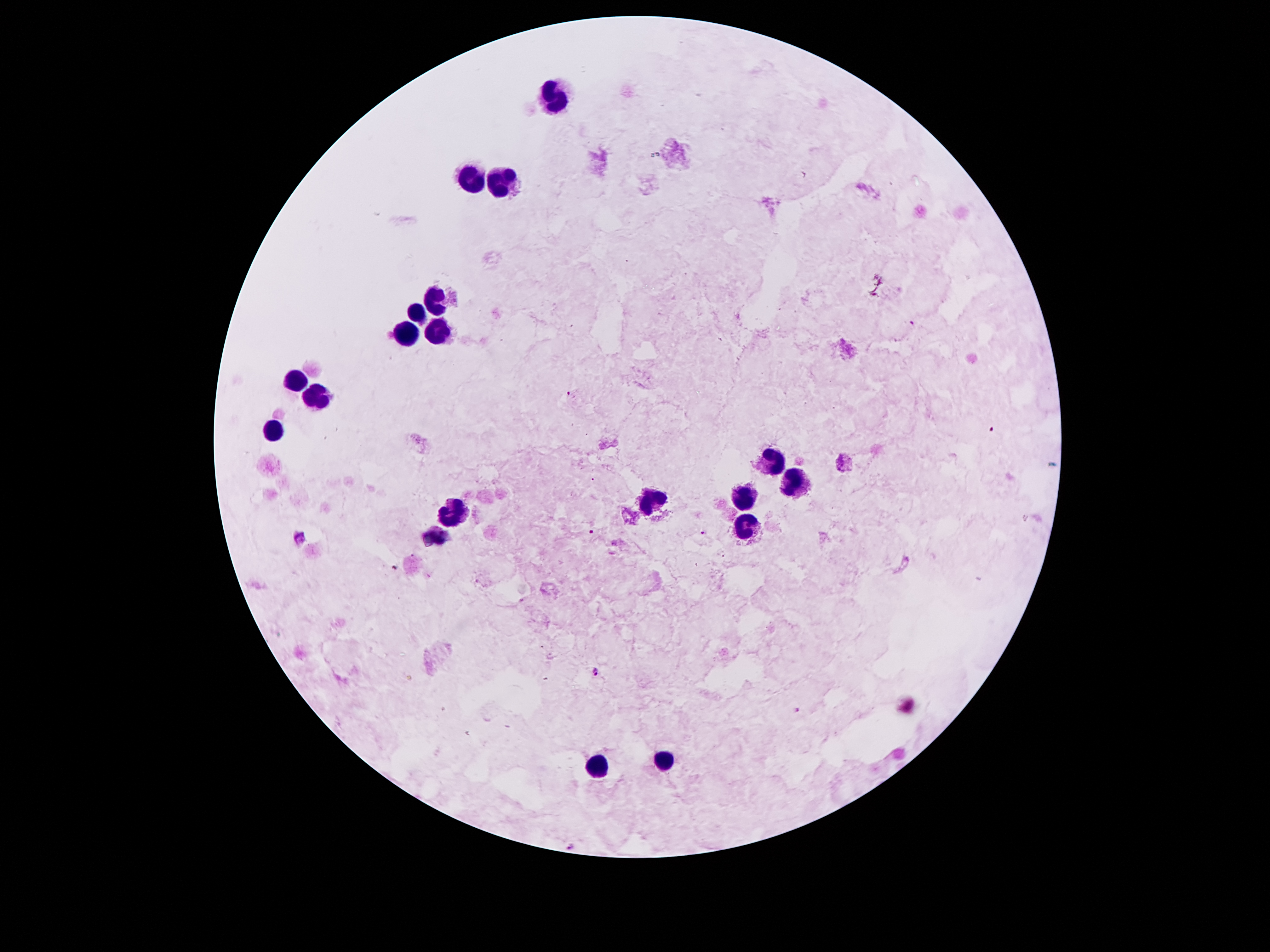

Approximate object centers, in pixels from the top-left corner. Plasmodium parasite locations: (x=912, y=324), (x=569, y=394), (x=990, y=429), (x=591, y=531), (x=702, y=534), (x=596, y=672), (x=798, y=711). Leukocyte locations: (x=554, y=98), (x=470, y=174), (x=505, y=187), (x=437, y=301), (x=413, y=315), (x=437, y=324), (x=406, y=333), (x=293, y=382), (x=315, y=399), (x=275, y=430), (x=768, y=459), (x=795, y=479), (x=746, y=496), (x=649, y=503), (x=453, y=510), (x=746, y=523), (x=432, y=537), (x=663, y=760), (x=596, y=769). Image is 1270×952 pixels. Thick blood film. Giemsa stain. Smartphone photograph taken through the microscope eyepiece. One field from this slide. Patient malaria status: positive for Plasmodium falciparum. 100x magnification.